State which parasite is depicted.
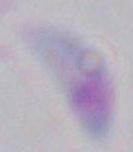

Toxoplasma gondii.

modality = micrograph
magnification = 1000x